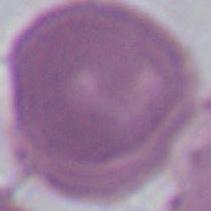
modality = photomicrograph
magnification = 1000x
identification = erythrocyte